State which parasite is depicted.
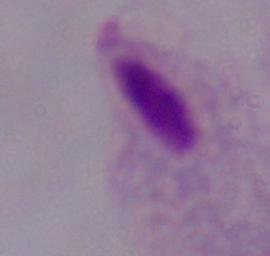
A trichomonad.

Summary:
  - Modality: photomicrograph
  - Magnification: 1000x